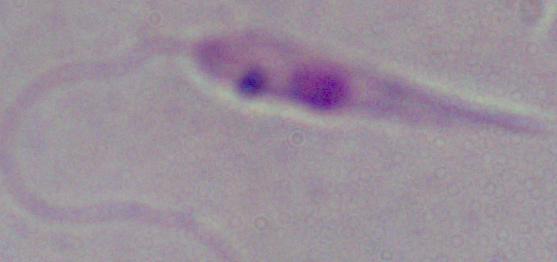
magnification = 1000x
identification = Leishmania
modality = micrograph